Report the malaria status of this cell.
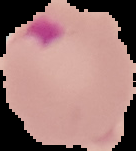
It is parasitized.

{
  "preparation": "thin blood smear",
  "image_type": "segmented cell region with the area outside set to black",
  "image_size": "136×151 pixels"
}